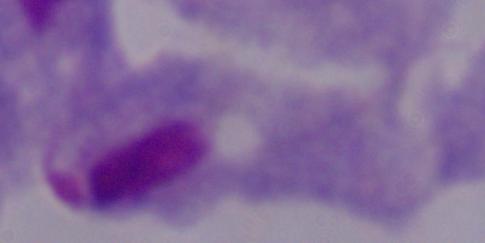

Summary:
  - Magnification: 1000x
  - Modality: photomicrograph
  - Identification: trichomonad